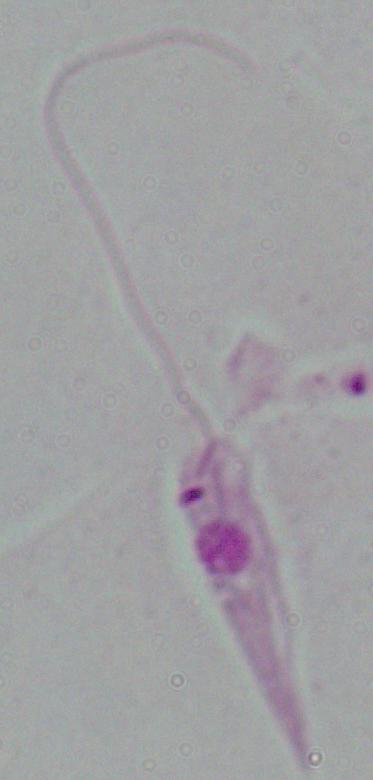

magnification = 1000x
modality = micrograph
identification = Leishmania